Point out each malaria parasite.
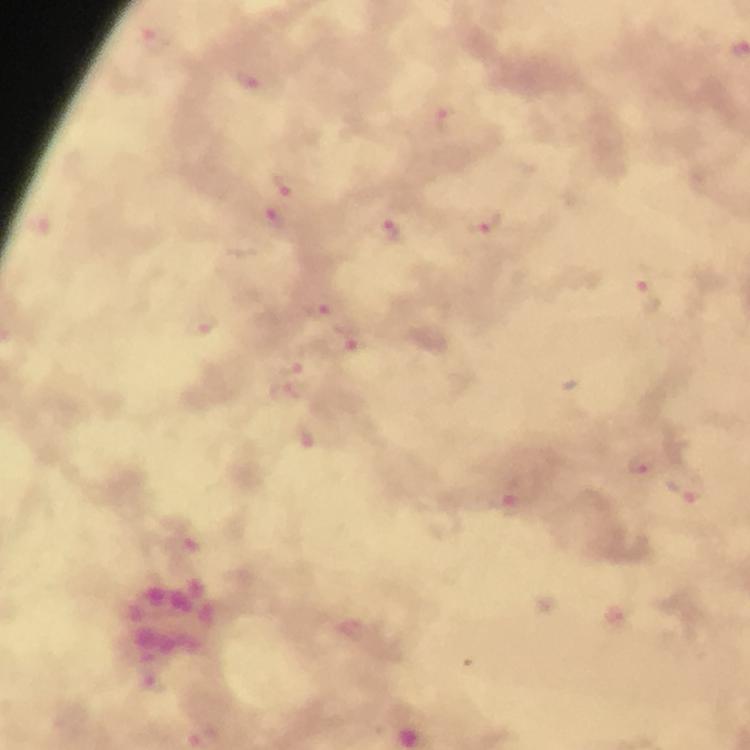
Approximate object centers, in pixels from the top-left corner.
Malaria parasites: (x=155, y=39), (x=248, y=79), (x=448, y=119), (x=293, y=186), (x=271, y=218), (x=484, y=221), (x=392, y=230), (x=647, y=294), (x=317, y=307), (x=201, y=324), (x=353, y=343), (x=290, y=382), (x=642, y=463), (x=687, y=487), (x=515, y=492), (x=186, y=546), (x=619, y=612).

Summary:
  - Magnification: 100x
  - Preparation: thick blood film
  - Cropped from: one field of view
  - Image size: 750×750 pixels
  - Immersion oil: applied
  - Stain: Giemsa
  - Capture: smartphone mounted on the microscope
  - Context: from a diagnostic examination for malaria